Comment on the morphology of the erythrocytes.
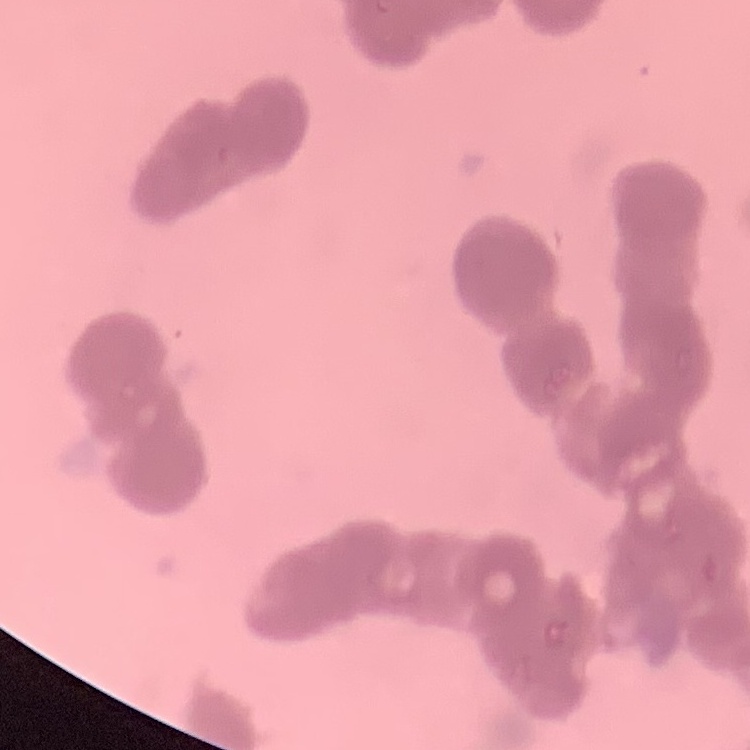
Rouleaux formation.

preparation = thin peripheral smear
image type = square crop of a larger photomicrograph
stain = Field's or Giemsa